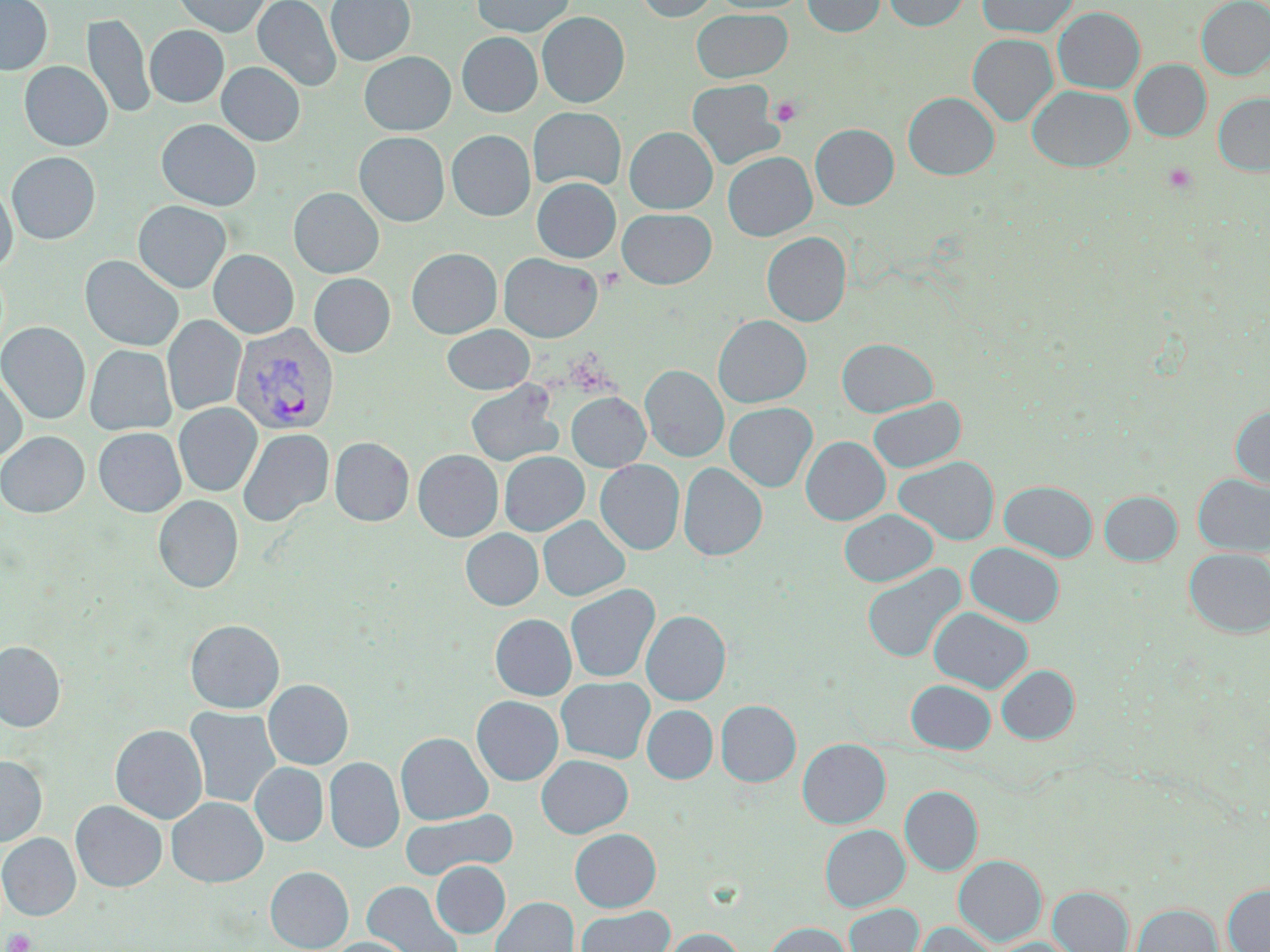
Approximate bounding boxes as (x1, y1, x2, y2) in pixels. Platelet locations: (769, 96, 802, 126), (1162, 163, 1198, 194), (4, 929, 37, 952). Uninfected red blood cell locations: (0, 0, 52, 75), (172, 0, 271, 36), (253, 0, 342, 91), (326, 0, 415, 66), (472, 0, 574, 36), (634, 0, 718, 21), (709, 0, 809, 14), (803, 0, 885, 36), (884, 0, 971, 30), (977, 0, 1078, 37), (1196, 0, 1270, 79), (1053, 7, 1145, 93), (692, 8, 792, 83), (537, 11, 629, 107), (83, 14, 154, 120), (145, 25, 229, 107), (457, 32, 542, 117), (967, 33, 1058, 126), (359, 52, 455, 135), (1130, 59, 1211, 141), (19, 61, 113, 151), (217, 62, 305, 146), (687, 79, 784, 169), (1027, 86, 1134, 171), (903, 92, 999, 179), (1213, 93, 1270, 175), (528, 107, 626, 191), (156, 119, 261, 211), (810, 124, 898, 210), (624, 126, 717, 213), (446, 130, 535, 220), (354, 132, 450, 226), (6, 151, 100, 244), (723, 151, 816, 241), (532, 177, 620, 263), (0, 183, 17, 271), (289, 187, 384, 278), (133, 200, 231, 293), (617, 208, 716, 288), (762, 232, 851, 326), (407, 248, 502, 338), (209, 249, 299, 338), (499, 253, 602, 342), (80, 255, 184, 351), (309, 273, 395, 357), (163, 315, 245, 416), (712, 315, 811, 407), (0, 321, 90, 424), (442, 324, 534, 395), (837, 338, 937, 417), (85, 344, 176, 436), (640, 365, 728, 462), (0, 371, 27, 463), (466, 381, 562, 467), (567, 392, 650, 471), (868, 396, 966, 473), (174, 402, 262, 496), (725, 402, 817, 491), (1230, 406, 1270, 489), (93, 427, 186, 517), (238, 428, 334, 527), (0, 431, 89, 517), (329, 436, 414, 526), (801, 436, 890, 524), (413, 450, 502, 541), (499, 451, 588, 536), (894, 456, 999, 545), (595, 459, 684, 555), (678, 462, 767, 560), (1194, 474, 1270, 556), (999, 480, 1097, 561), (1099, 491, 1181, 565), (153, 494, 243, 592), (839, 509, 938, 586), (538, 516, 629, 601), (461, 528, 542, 610), (966, 543, 1064, 626), (1184, 548, 1270, 637), (861, 563, 967, 663), (565, 584, 660, 683), (929, 607, 1033, 693), (642, 610, 731, 705), (490, 614, 576, 700), (185, 619, 285, 713), (0, 640, 65, 732), (996, 664, 1079, 744), (556, 676, 655, 763), (264, 679, 353, 769), (906, 679, 996, 753), (472, 696, 563, 785), (715, 700, 801, 786), (642, 705, 718, 783), (185, 706, 280, 809), (110, 724, 207, 824), (395, 732, 493, 825), (797, 738, 891, 828), (536, 754, 633, 838), (0, 755, 47, 846), (324, 757, 404, 853), (250, 762, 328, 846), (900, 786, 983, 875), (167, 797, 267, 887), (71, 801, 166, 891), (400, 808, 518, 880), (820, 824, 909, 911), (569, 828, 661, 912), (0, 833, 81, 920), (953, 855, 1047, 945), (432, 861, 510, 938), (265, 866, 353, 952), (362, 881, 464, 952), (1223, 884, 1270, 952), (1048, 886, 1134, 952), (491, 897, 579, 952), (844, 903, 924, 952), (1131, 903, 1222, 952), (576, 906, 675, 952), (913, 921, 997, 952), (765, 922, 852, 952), (660, 927, 746, 952), (327, 937, 414, 952), (991, 937, 1078, 952). Plasmodium vivax-infected red blood cell locations: (230, 321, 339, 435). Slide-level diagnosis: Plasmodium vivax. Optical microscopy. May-Grünwald-Giemsa stain. Captured at 1000x magnification. Thin blood film. Image is 1270×952 pixels. One field of a larger specimen.